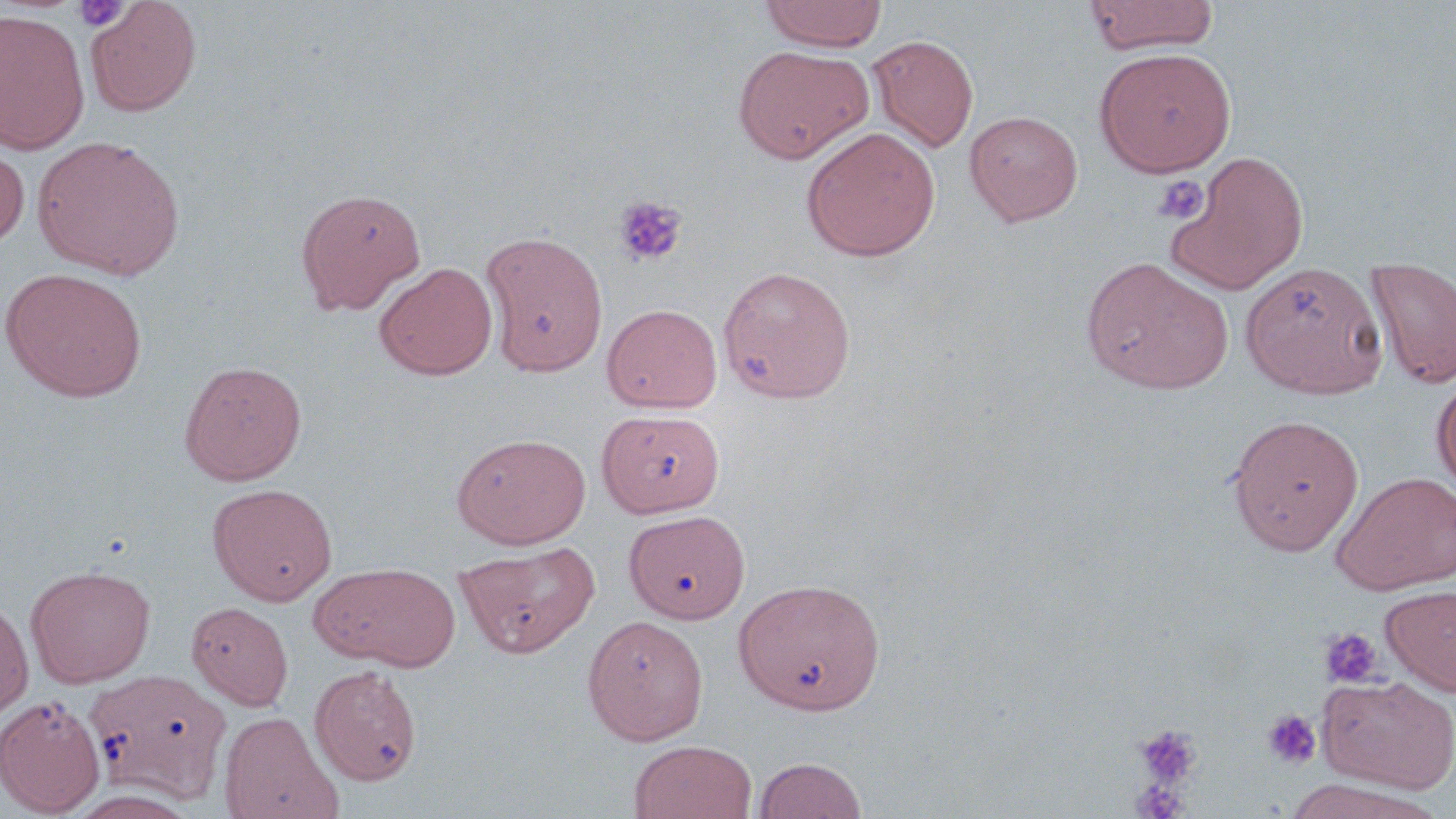

slide-level diagnosis = no evidence of blood parasites
image size = 1456×819 pixels
magnification = 1000x
preparation = thin blood smear
uninfected red blood cell locations = approximate bounding boxes as named x1/y1/x2/y2 corners in pixels: (x1=86, y1=0, x2=202, y2=117), (x1=759, y1=0, x2=888, y2=52), (x1=1084, y1=0, x2=1221, y2=55), (x1=0, y1=9, x2=90, y2=155), (x1=867, y1=35, x2=979, y2=153), (x1=733, y1=45, x2=874, y2=164), (x1=1094, y1=47, x2=1237, y2=177), (x1=965, y1=110, x2=1083, y2=226), (x1=801, y1=127, x2=940, y2=261), (x1=32, y1=135, x2=185, y2=280), (x1=0, y1=145, x2=29, y2=248), (x1=1163, y1=150, x2=1309, y2=294), (x1=296, y1=187, x2=426, y2=314), (x1=481, y1=231, x2=608, y2=376), (x1=1081, y1=257, x2=1233, y2=394), (x1=1366, y1=257, x2=1456, y2=389), (x1=1240, y1=261, x2=1387, y2=399), (x1=374, y1=262, x2=498, y2=380), (x1=718, y1=265, x2=856, y2=403), (x1=0, y1=267, x2=148, y2=402), (x1=602, y1=303, x2=723, y2=413), (x1=178, y1=360, x2=307, y2=486), (x1=1431, y1=376, x2=1456, y2=494), (x1=598, y1=409, x2=724, y2=518), (x1=1227, y1=413, x2=1365, y2=556), (x1=451, y1=432, x2=591, y2=548), (x1=1331, y1=472, x2=1456, y2=595), (x1=207, y1=482, x2=337, y2=605), (x1=624, y1=510, x2=749, y2=624), (x1=455, y1=540, x2=601, y2=658), (x1=309, y1=562, x2=460, y2=671), (x1=26, y1=564, x2=156, y2=687), (x1=734, y1=577, x2=886, y2=715), (x1=1381, y1=584, x2=1456, y2=696), (x1=0, y1=595, x2=34, y2=720), (x1=186, y1=601, x2=293, y2=710), (x1=583, y1=615, x2=709, y2=744), (x1=309, y1=664, x2=423, y2=786), (x1=85, y1=669, x2=231, y2=803), (x1=1318, y1=675, x2=1455, y2=793), (x1=0, y1=695, x2=105, y2=816), (x1=219, y1=711, x2=342, y2=819), (x1=628, y1=739, x2=757, y2=819), (x1=752, y1=757, x2=868, y2=818), (x1=1280, y1=777, x2=1441, y2=819)
field of view = one of a larger specimen
platelet locations = approximate bounding boxes as named x1/y1/x2/y2 corners in pixels: (x1=72, y1=1, x2=130, y2=32), (x1=1152, y1=174, x2=1210, y2=226), (x1=613, y1=196, x2=687, y2=267), (x1=1320, y1=627, x2=1383, y2=689), (x1=1261, y1=709, x2=1323, y2=772), (x1=1133, y1=723, x2=1202, y2=791), (x1=1128, y1=779, x2=1191, y2=819)
modality = optical microscopy
stain = May-Grünwald-Giemsa